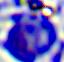
Micrograph. 400x magnification. A leukocyte is seen.